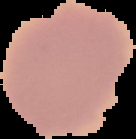

malaria status = uninfected
image type = segmented cell region with the area outside set to black
image size = 136×139 pixels
preparation = thin blood film